Name the parasite shown.
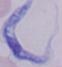
This is a trypanosome.

Micrograph. Captured at 1000x magnification.